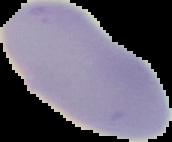
{
  "preparation": "thin blood film",
  "image_size": "172×142 pixels",
  "image_type": "segmented cell region with the area outside set to black",
  "malaria_status": "uninfected"
}